Assess for malaria.
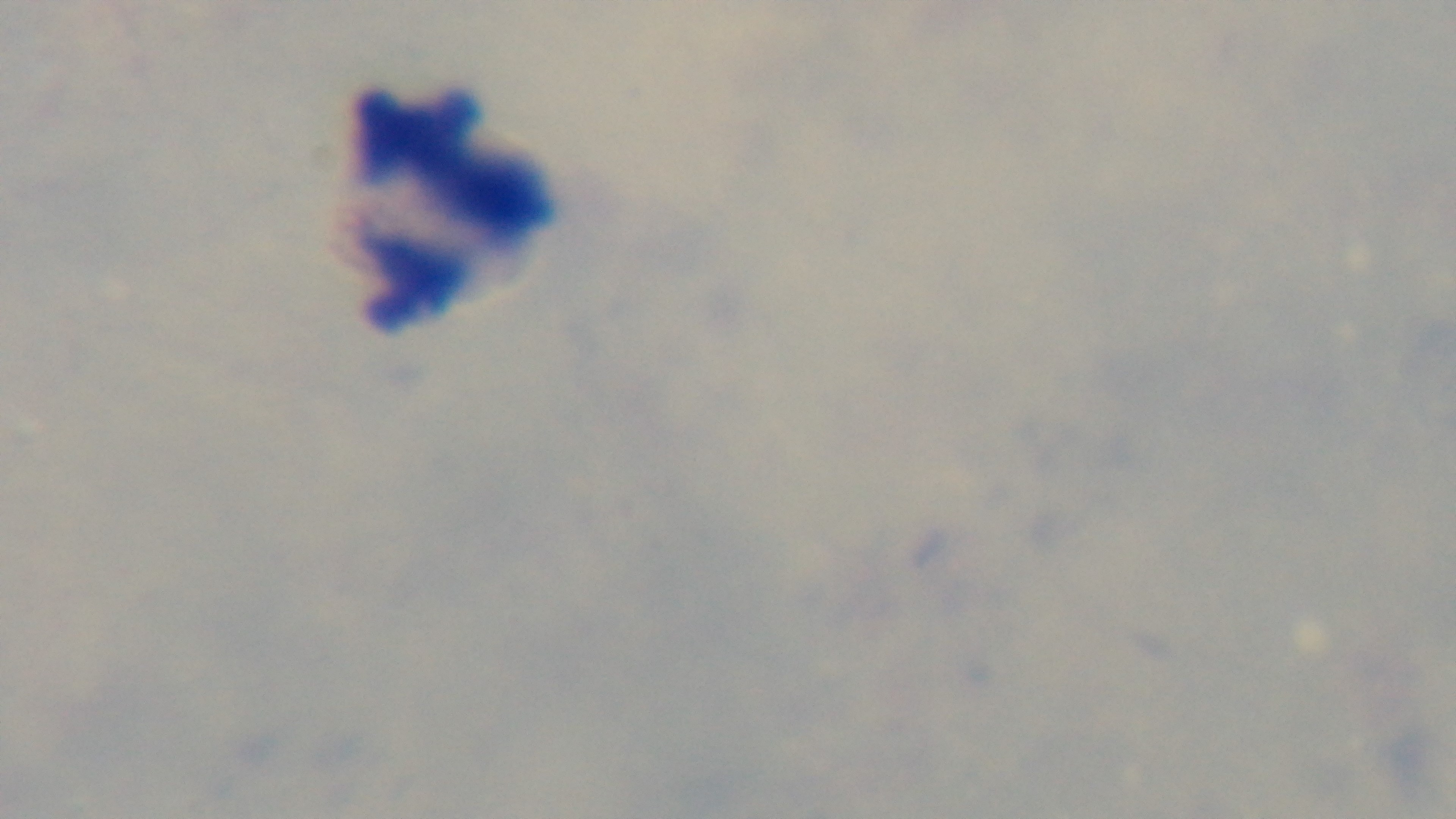

It is uninfected.

objective: 100x oil immersion
stain: Giemsa
modality: light microscopy
field_of_view: one from the slide
preparation: thick smear
capture: mounted 4K digital camera